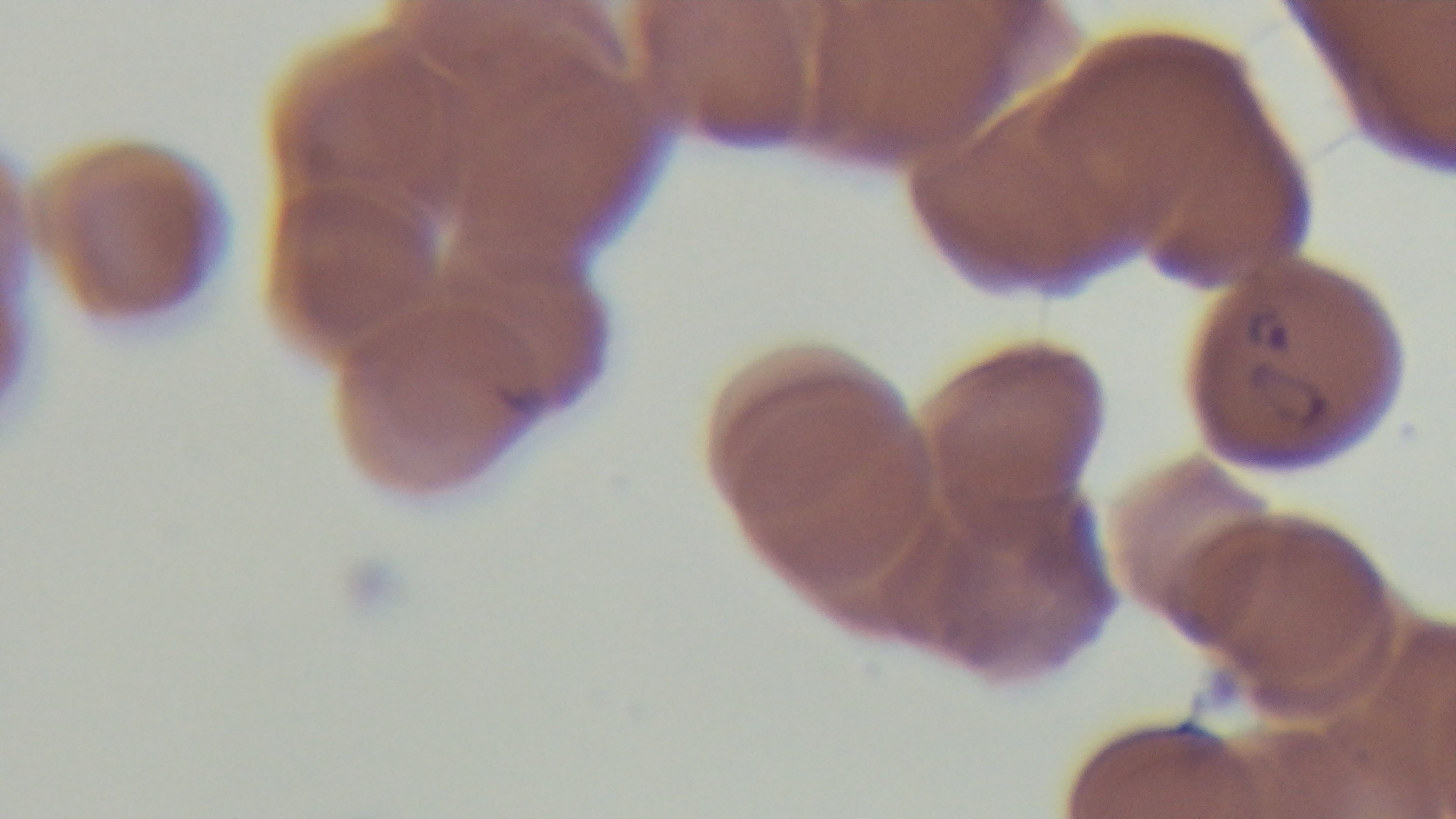

objective = 100x oil immersion
modality = light microscopy
field of view = single
capture = mounted 4K digital camera
preparation = thin blood film
stain = Giemsa
malaria status = positive